Name the parasite shown.
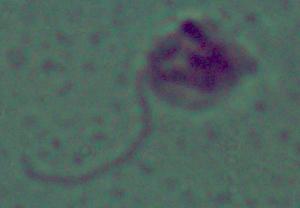

Leishmania.

Captured at 1000x magnification. Photomicrograph.